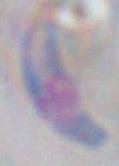
1000x magnification. Photomicrograph. Toxoplasma gondii is seen.